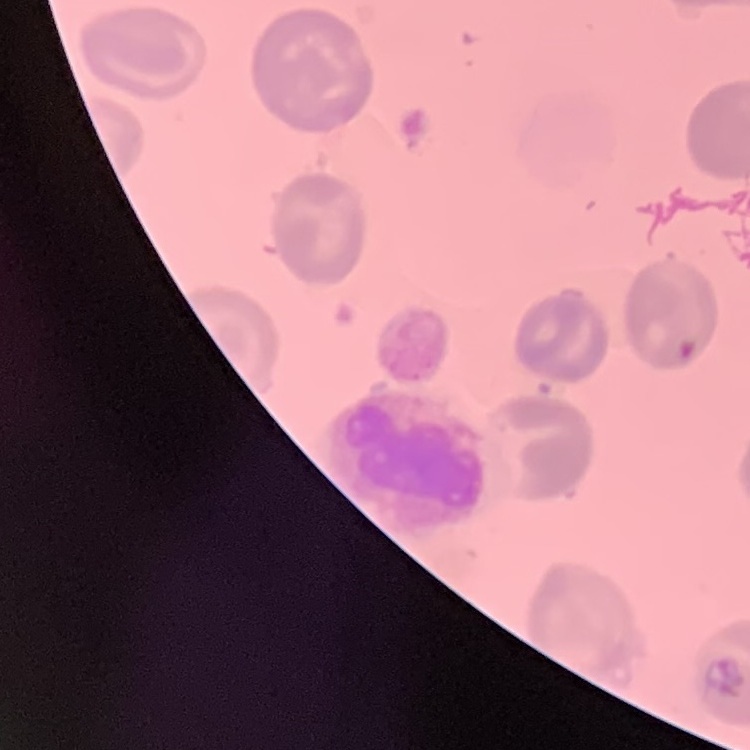

{
  "red_blood_cell_morphology": "no rouleaux formation",
  "stain": "Field's or Giemsa",
  "image_type": "square crop of a larger photomicrograph",
  "preparation": "thin peripheral smear"
}